Report the malaria status of this cell.
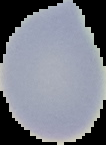

Uninfected.

Image is 106×145 pixels. From a thin blood smear. Cell region segmented out of the field of view; the surrounding area is masked to black.